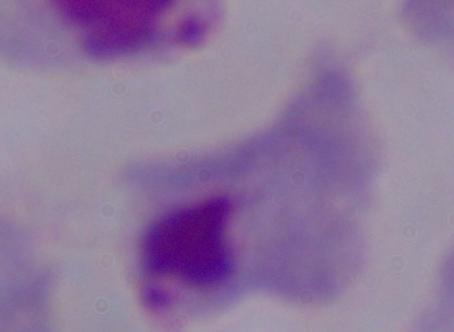

Summary:
  - Modality: micrograph
  - Identification: trichomonad
  - Magnification: 1000x